Describe the morphology of the red blood cells.
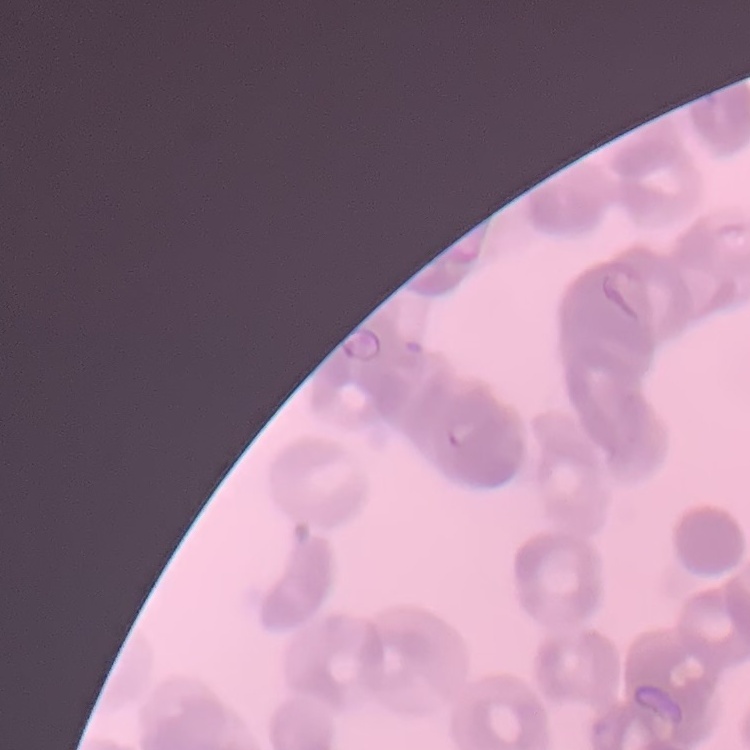

They show rouleaux formation.

One tile cut from a larger photomicrograph. Thin blood smear. Field's or Giemsa stain.